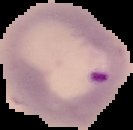
Image is 133×130 pixels. Result: malaria parasites identified. From a thin blood smear. Cell region segmented out of the field of view; the surrounding area is masked to black.